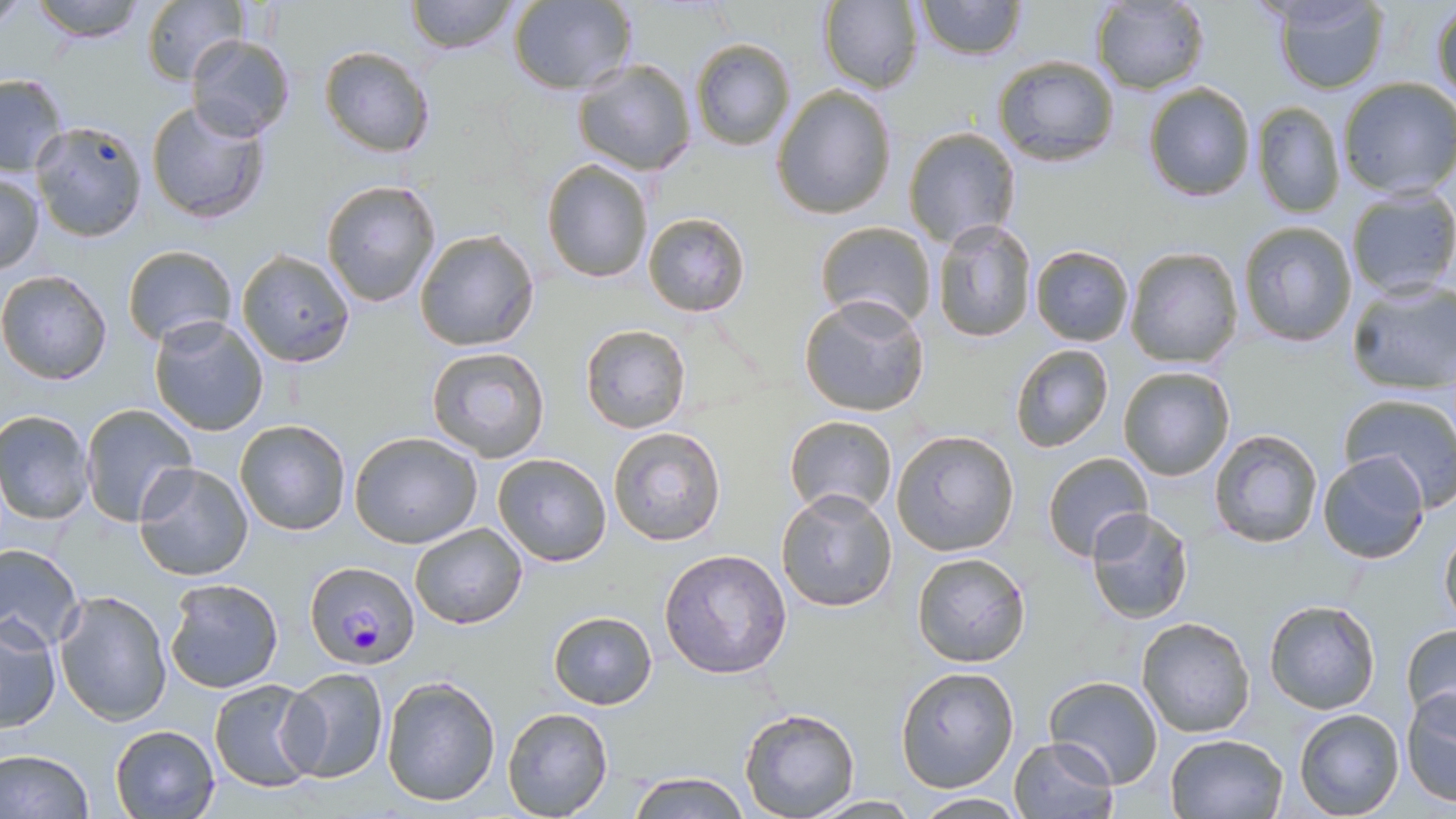
Approximate bounding boxes as (x1, y1, x2, y2) in pixels. Plasmodium falciparum-infected red blood cell locations: (304, 561, 417, 669). Uninfected red blood cell locations: (27, 0, 148, 43), (406, 0, 521, 54), (509, 0, 638, 94), (915, 0, 1026, 61), (1267, 0, 1391, 93), (1, 1, 27, 34), (817, 1, 926, 93), (1087, 1, 1210, 94), (1429, 1, 1456, 110), (141, 3, 243, 84), (186, 34, 296, 140), (689, 37, 794, 152), (317, 45, 435, 160), (991, 55, 1121, 169), (572, 59, 697, 176), (0, 72, 68, 175), (1337, 77, 1456, 198), (1142, 81, 1255, 202), (771, 83, 896, 218), (145, 99, 270, 225), (1251, 102, 1345, 217), (30, 119, 148, 242), (903, 129, 1020, 248), (542, 160, 652, 283), (1, 170, 45, 274), (320, 180, 440, 307), (1345, 188, 1456, 299), (642, 212, 752, 317), (930, 218, 1037, 344), (815, 221, 936, 332), (1237, 221, 1359, 348), (414, 228, 540, 352), (120, 244, 237, 348), (1030, 245, 1134, 345), (1125, 246, 1244, 368), (236, 249, 356, 368), (0, 270, 114, 385), (1346, 278, 1456, 394), (799, 295, 931, 418), (148, 315, 269, 436), (579, 323, 692, 434), (1009, 343, 1113, 453), (426, 344, 550, 460), (1117, 366, 1234, 480), (1338, 391, 1456, 507), (80, 404, 199, 527), (0, 408, 94, 525), (784, 415, 897, 519), (234, 418, 352, 536), (607, 426, 727, 547), (1208, 428, 1326, 549), (891, 430, 1019, 557), (349, 431, 482, 549), (1316, 450, 1431, 565), (1042, 451, 1152, 564), (492, 453, 612, 567), (133, 462, 254, 582), (774, 486, 899, 612), (1085, 507, 1194, 624), (408, 524, 528, 630), (1439, 524, 1456, 629), (0, 543, 84, 652), (659, 547, 792, 681), (911, 551, 1032, 669), (162, 577, 286, 694), (54, 588, 173, 726), (1264, 599, 1380, 714), (548, 610, 658, 710), (1135, 615, 1256, 739), (1, 616, 61, 733), (1401, 623, 1456, 724), (894, 666, 1019, 791), (279, 667, 389, 784), (380, 675, 503, 807), (1043, 676, 1163, 789), (207, 679, 321, 793), (1401, 686, 1456, 805), (502, 705, 612, 818), (738, 707, 860, 819), (1293, 708, 1404, 819), (110, 725, 220, 817), (1165, 732, 1288, 819), (1009, 736, 1119, 819), (0, 749, 95, 819), (630, 770, 748, 818), (912, 793, 1025, 818), (806, 794, 922, 817). Slide-level diagnosis: Plasmodium falciparum. Image is 1456×819 pixels. May-Grünwald-Giemsa stain. Light microscopy. Single field of view. Thin blood film. 1000x magnification.